Report the malaria status of this cell.
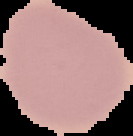

Uninfected.

{
  "image_size": "133×136 pixels",
  "preparation": "thin blood film",
  "image_type": "segmented cell region on a black background"
}